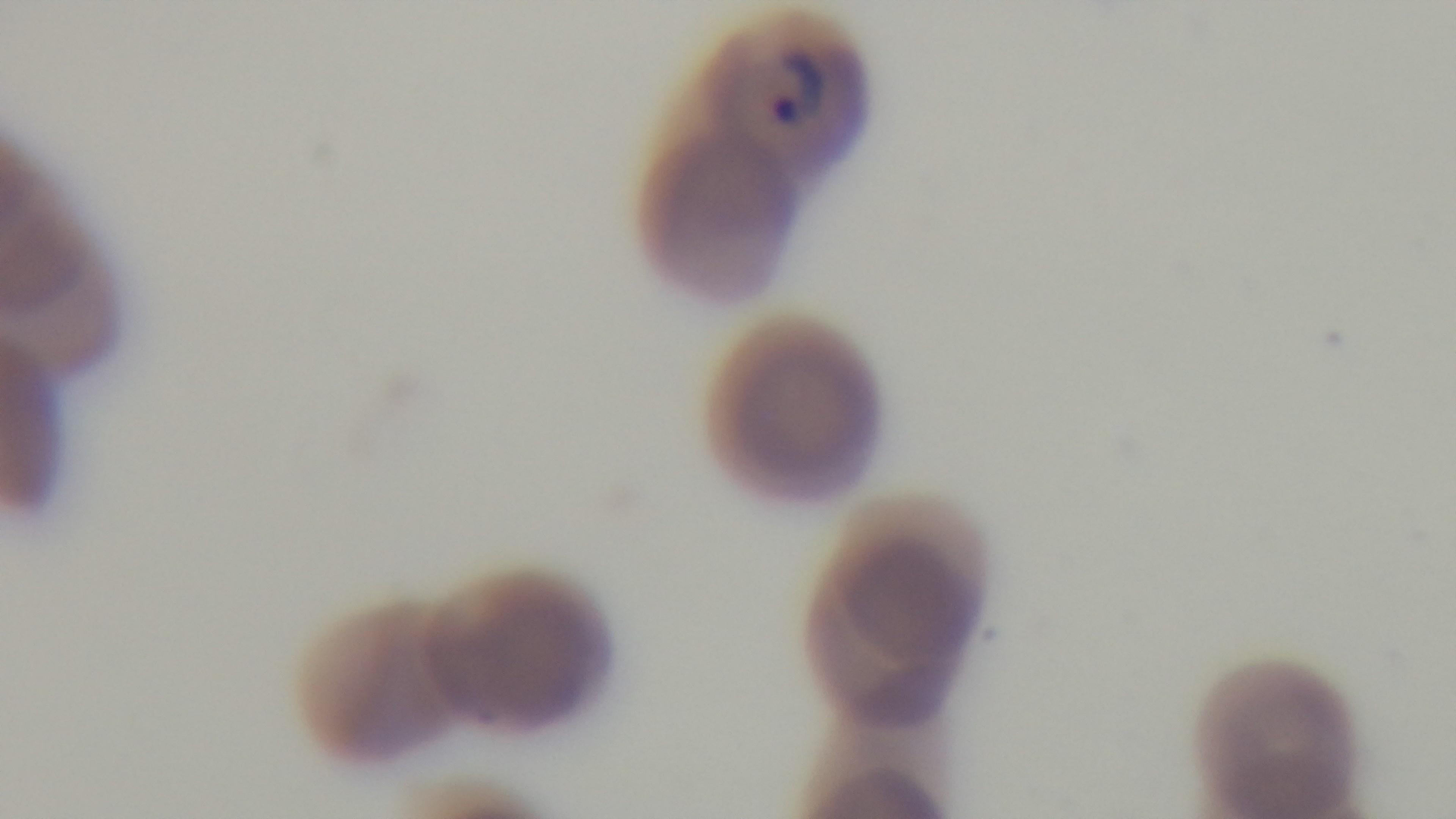 Mounted 4K digital camera. Malaria status: positive. 100x oil-immersion objective. Giemsa-stained. Photomicrograph. Preparation: thin. One field from the slide.